Locate every malaria parasite.
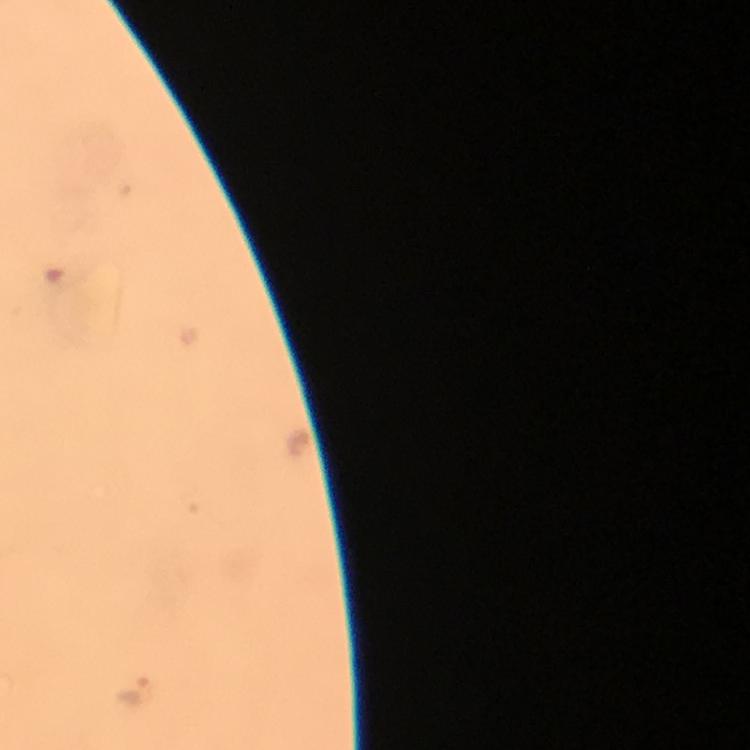

Approximate centers as (x, y) in pixels.
Malaria parasites: (131, 688).

Summary:
  - Preparation: thick blood film
  - Image size: 750×750 pixels
  - Cropped from: one field of view
  - Stain: Giemsa
  - Capture: smartphone camera through the microscope
  - Magnification: 100x
  - Context: from a malaria diagnostic workup
  - Immersion oil: applied